Classify this cell by malaria status.
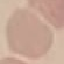
Uninfected.

Summary:
  - Preparation: thin blood film
  - Capture: smartphone camera at the microscope eyepiece
  - Stain: Giemsa
  - Image type: cell patch, automatically extracted from a larger field of view and resized to 64 × 64 pixels